Classify this cell by malaria status.
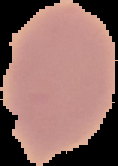
Uninfected.

Cell region segmented out of the field of view; the surrounding area is masked to black. From a thin blood smear. Image is 118×166 pixels.